Point out each malaria parasite and each leukocyte.
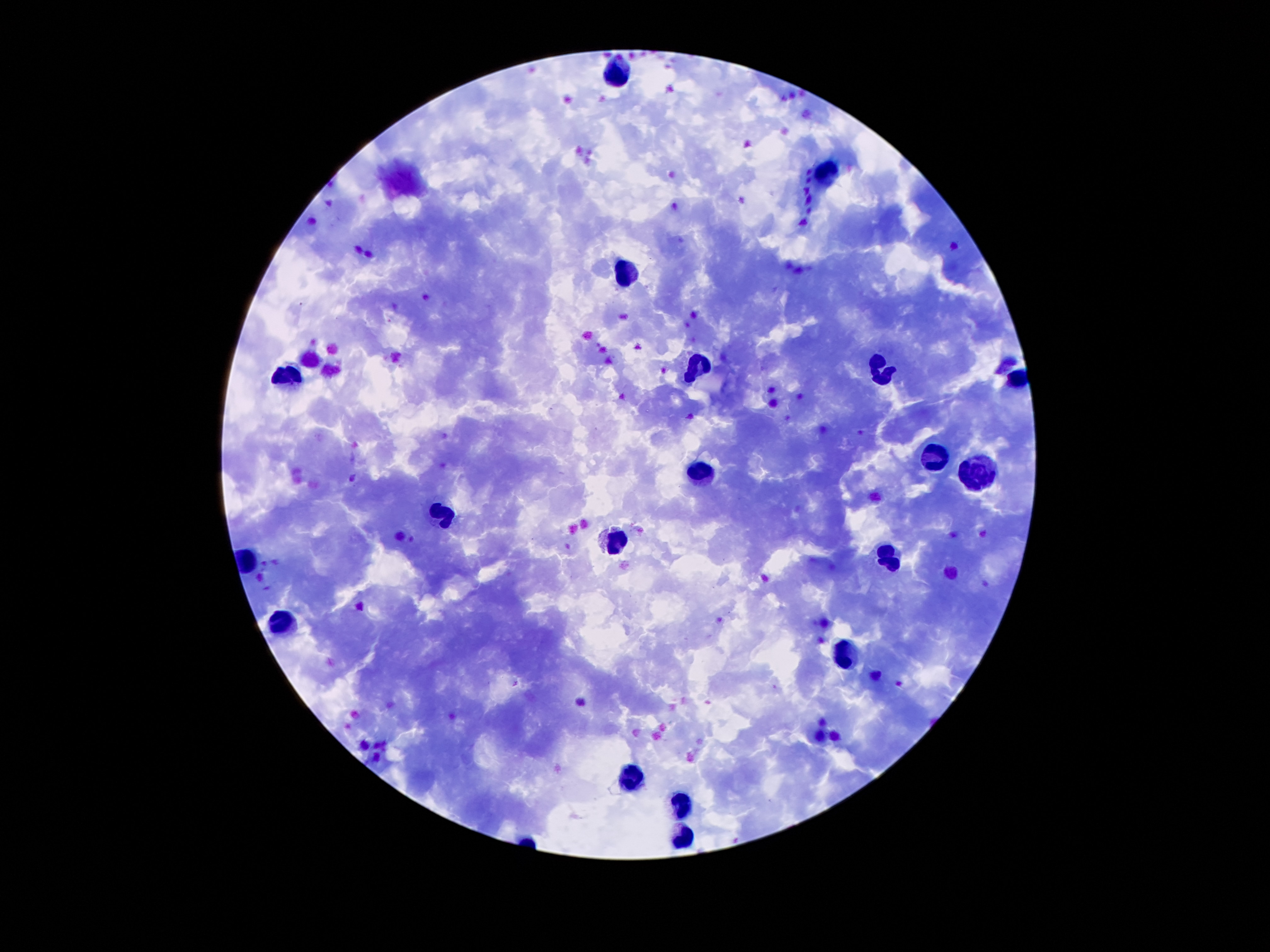

Approximate centers as {x, y} in pixels.
Malaria parasites: {353, 478}, {517, 684}.
Leukocytes: {619, 69}, {823, 173}, {629, 273}, {694, 367}, {881, 367}, {280, 374}, {933, 460}, {697, 469}, {978, 470}, {442, 514}, {616, 541}, {887, 556}, {283, 621}, {842, 654}, {632, 774}, {681, 805}, {684, 837}.

Summary:
  - Image size: 1270×952 pixels
  - Capture: smartphone through the microscope eyepiece
  - Patient malaria status: positive for Plasmodium falciparum
  - Stain: Giemsa
  - Magnification: 100x
  - Field of view: single
  - Preparation: thick blood smear